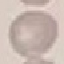

Malaria status: uninfected. Acquired by smartphone through the microscope eyepiece. Thin blood film. Automatically extracted cell patch, resized to 64 × 64 pixels. Giemsa stain.